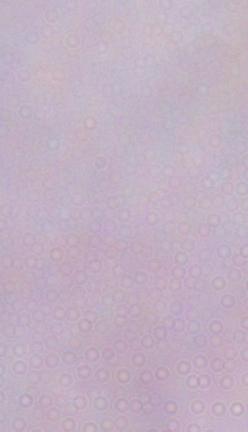
Captured at 1000x magnification. Photomicrograph. A trypanosome is seen.